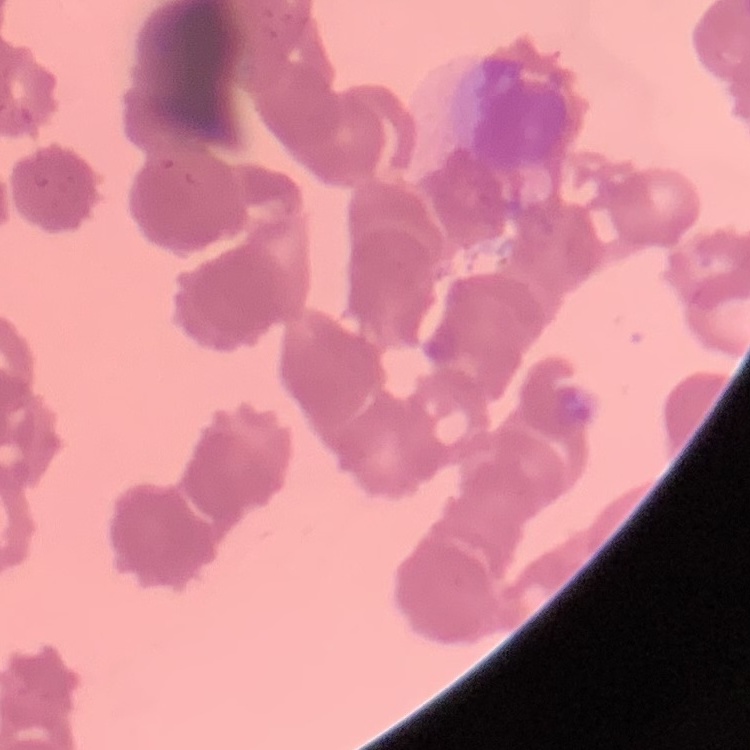

Summary:
  - Red blood cell morphology: rouleaux formation
  - Image type: square crop of a larger photomicrograph
  - Stain: Field's or Giemsa
  - Preparation: thin blood film